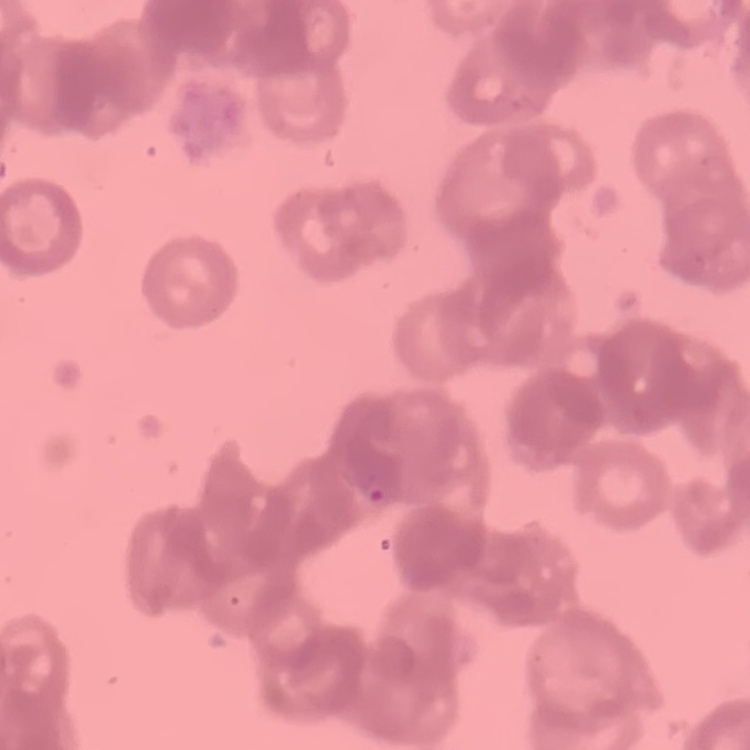

Summary:
  - Red blood cell morphology: rouleaux formation
  - Stain: Field's or Giemsa
  - Image type: square crop of a larger photomicrograph
  - Preparation: thin blood film